Give the position of every leukocyte visible.
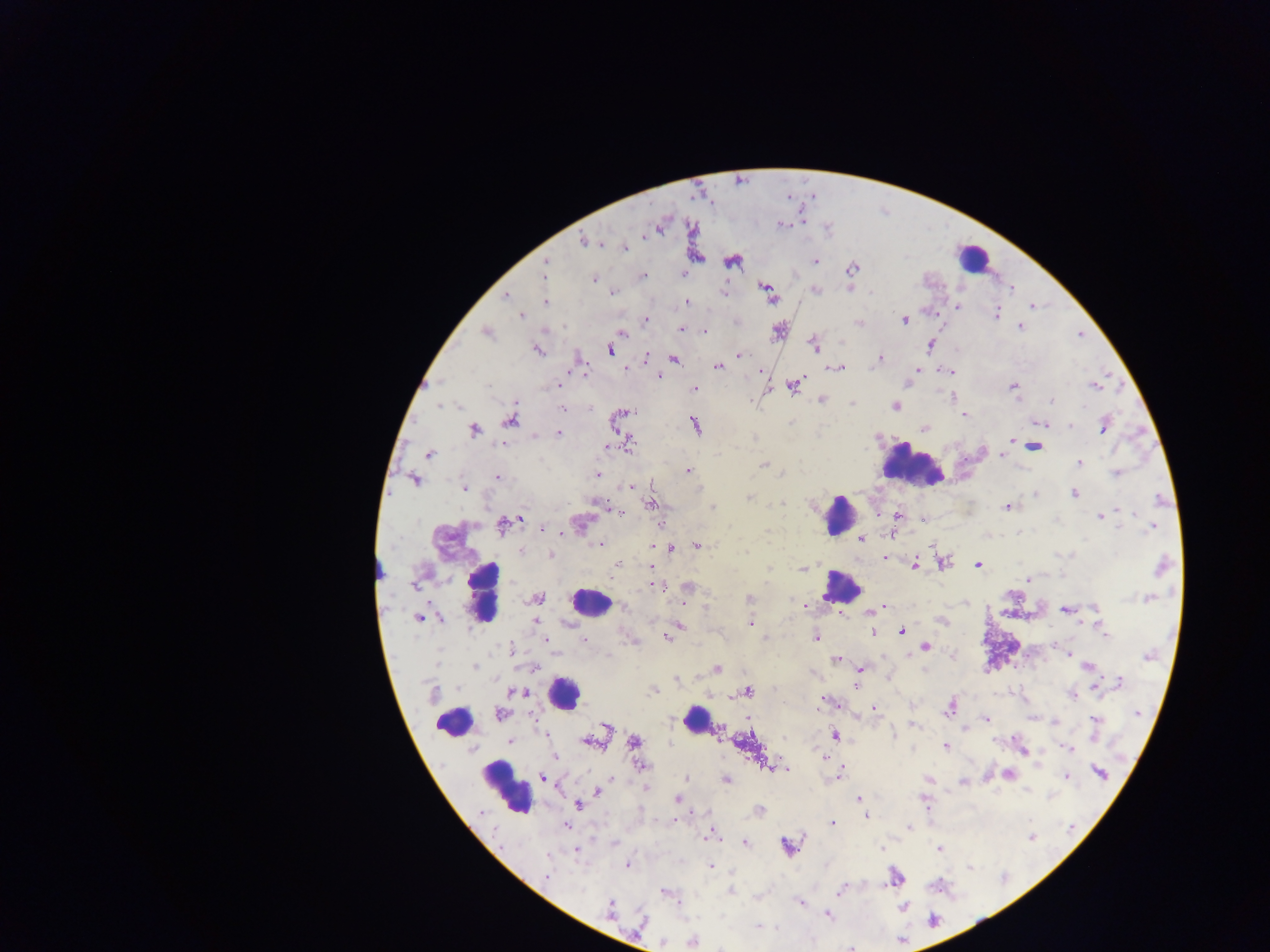

Approximate centers as (x, y) in pixels.
Leukocytes: (972, 259), (910, 463), (837, 515), (841, 586), (481, 592), (590, 602), (562, 693), (695, 719), (454, 721), (505, 786).

Summary:
  - Plasmodium parasite locations: (662, 223), (645, 235), (584, 241), (624, 247), (732, 260), (815, 262), (545, 265), (851, 269), (684, 275), (543, 276), (643, 276), (594, 278), (766, 287), (851, 288), (1011, 289), (814, 290), (612, 291), (724, 292), (505, 296), (771, 297), (686, 301), (545, 302), (1031, 304), (957, 306), (995, 314), (521, 315), (905, 319), (644, 320), (860, 322), (1020, 327), (681, 329), (702, 329), (778, 330), (486, 332), (621, 333), (814, 345), (930, 345), (536, 349), (609, 349), (738, 355), (645, 359), (674, 359), (878, 359), (718, 366), (837, 367), (624, 368), (916, 368), (761, 369), (583, 371), (949, 371), (658, 376), (562, 382), (794, 384), (559, 386), (1013, 386), (1094, 386), (694, 388), (1052, 399), (821, 400), (516, 401), (852, 403), (894, 406), (562, 409), (626, 412), (964, 415), (618, 419), (510, 420), (1041, 423), (695, 425), (1068, 425), (1103, 426), (924, 427), (473, 429), (558, 432), (1011, 440), (629, 445), (1033, 447), (607, 448), (429, 453), (1003, 455), (1079, 463), (763, 465), (687, 470), (1116, 473), (597, 474), (498, 477), (414, 479), (630, 486), (463, 487), (1074, 493), (1035, 494), (595, 502), (651, 504), (1007, 506), (612, 511), (617, 511), (1116, 511), (877, 513), (898, 515), (1100, 516), (518, 518), (922, 518), (580, 524), (503, 525), (1153, 527), (543, 529), (548, 530), (890, 534), (860, 538), (599, 543), (697, 544), (654, 545), (671, 549), (520, 551), (551, 555), (885, 558), (941, 563), (618, 564), (917, 564), (913, 565), (977, 565), (1161, 566), (652, 567), (803, 568), (613, 571), (1028, 579), (417, 583), (659, 586), (687, 587), (537, 598), (1147, 598), (749, 599), (805, 606), (623, 607), (884, 607), (1065, 610), (870, 612), (838, 614), (418, 617), (942, 620), (535, 621), (750, 623), (1098, 623), (679, 625), (873, 632), (901, 632), (666, 637), (816, 637), (765, 638), (546, 639), (582, 639), (924, 646), (510, 651), (1068, 654), (836, 659), (1088, 666), (716, 668), (859, 668), (677, 679), (1118, 682), (855, 684), (1100, 684), (654, 690), (746, 691), (517, 692), (433, 693), (1072, 694), (709, 696), (823, 702), (837, 703), (949, 707), (873, 709), (499, 713), (748, 718), (986, 718), (1033, 718), (1095, 719), (912, 724), (606, 729), (545, 733), (835, 736), (511, 740), (588, 742), (635, 742), (945, 745), (1070, 749), (1023, 750), (555, 756), (823, 757), (639, 766), (770, 768), (788, 769), (1008, 773), (1099, 773), (839, 775), (1067, 776), (543, 778), (687, 778), (929, 779), (726, 780), (964, 782), (646, 788), (597, 792), (677, 798), (858, 798), (925, 801), (578, 805), (759, 810), (866, 815), (673, 820), (831, 822), (566, 826), (909, 827), (707, 836), (1031, 836), (745, 843), (615, 844), (787, 846), (940, 849), (576, 850), (628, 864), (709, 867), (895, 876), (546, 877), (842, 888), (730, 891), (664, 892), (801, 902), (902, 907), (610, 910), (828, 914), (758, 925), (692, 940), (662, 941)
  - Capture: mobile-phone photograph through a microscope
  - Field of view: single
  - Image size: 1270×952 pixels
  - Country: Ghana
  - Preparation: thick blood smear